Locate and identify every blood parasite.
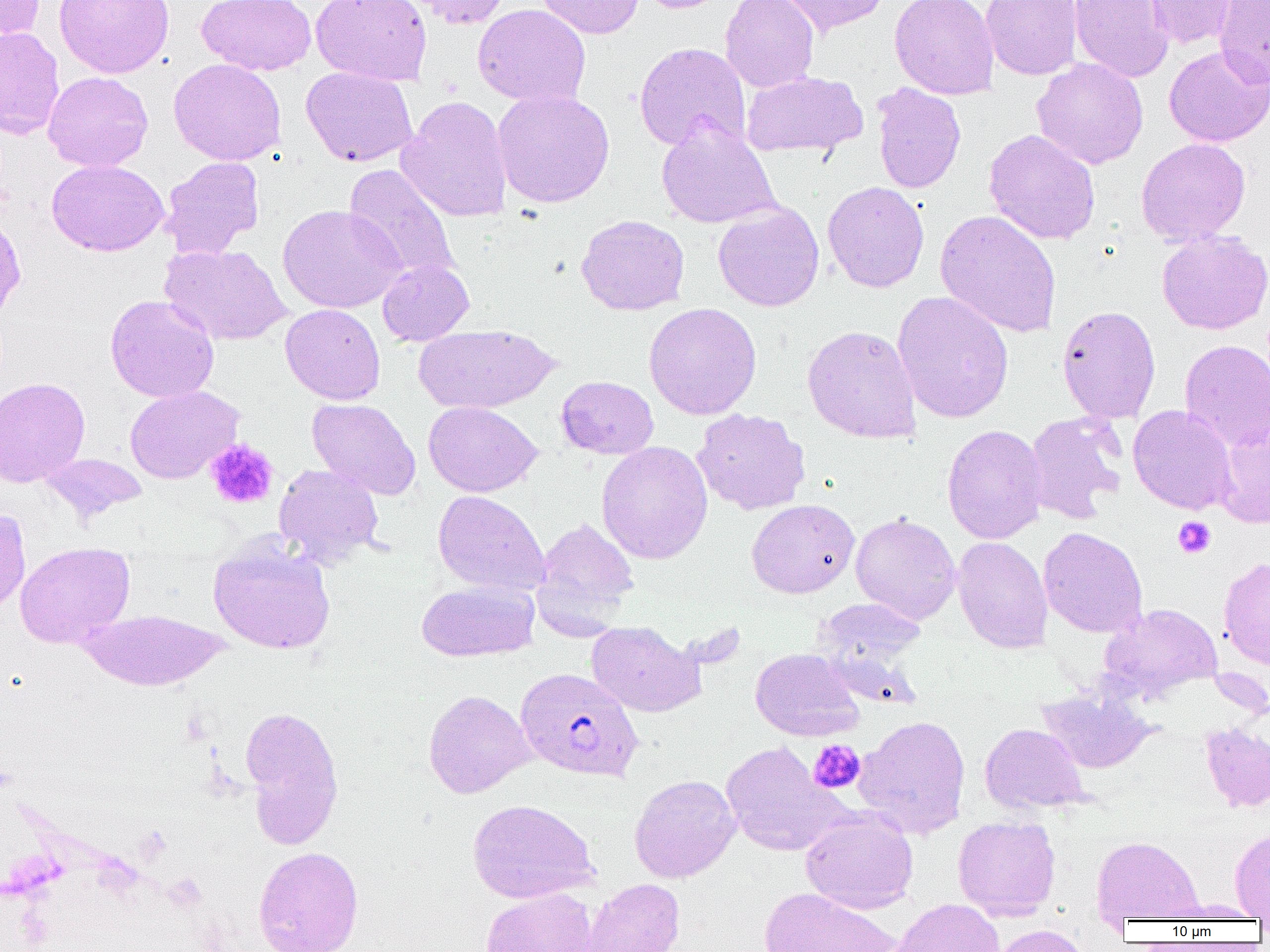
Approximate bounding boxes as (x1, y1, x2, y2) in pixels.
Plasmodium falciparum-infected red blood cells: (515, 667, 644, 782).
No Plasmodium ovale, Plasmodium malariae, Plasmodium vivax, Babesia divergens, or Trypanosoma brucei observed.

Uninfected red blood cell locations: (1, 0, 45, 42), (54, 0, 175, 79), (196, 0, 317, 76), (310, 0, 432, 86), (402, 0, 513, 29), (536, 0, 644, 38), (635, 0, 735, 14), (721, 0, 819, 92), (774, 0, 891, 37), (889, 0, 1000, 100), (981, 0, 1083, 80), (1070, 0, 1174, 83), (1145, 0, 1238, 49), (1214, 0, 1270, 88), (472, 4, 591, 108), (0, 27, 65, 139), (634, 42, 751, 151), (1163, 45, 1270, 147), (1031, 57, 1149, 170), (168, 58, 286, 165), (300, 66, 418, 167), (42, 71, 153, 172), (742, 71, 867, 157), (872, 82, 966, 193), (493, 88, 615, 208), (397, 95, 513, 222), (656, 120, 780, 228), (984, 129, 1100, 245), (1135, 137, 1251, 247), (160, 156, 265, 259), (47, 160, 169, 257), (343, 164, 461, 285), (822, 181, 929, 293), (713, 201, 824, 312), (277, 204, 406, 313), (934, 209, 1062, 338), (576, 214, 690, 316), (1156, 229, 1270, 335), (160, 243, 291, 346), (377, 259, 474, 345), (892, 290, 1014, 423), (105, 294, 219, 403), (643, 302, 762, 420), (280, 303, 385, 405), (1056, 305, 1161, 424), (414, 324, 561, 414), (802, 324, 922, 443), (1179, 339, 1270, 450), (556, 375, 659, 459), (0, 376, 90, 488), (124, 385, 243, 484), (307, 398, 421, 500), (423, 401, 543, 497), (1128, 404, 1238, 515), (692, 408, 811, 515), (1024, 411, 1127, 523), (1215, 421, 1270, 528), (942, 424, 1047, 544), (596, 441, 713, 564), (40, 453, 147, 522), (273, 463, 384, 566), (432, 489, 550, 595), (746, 499, 859, 599), (0, 507, 31, 615), (850, 513, 961, 625), (533, 516, 639, 633), (1038, 527, 1148, 638), (208, 536, 336, 655), (952, 536, 1053, 654), (14, 542, 135, 648), (1218, 556, 1270, 671), (416, 581, 539, 661), (813, 598, 926, 673), (1100, 603, 1223, 701), (80, 608, 229, 691), (586, 621, 706, 718), (750, 648, 864, 741), (1036, 688, 1156, 774), (423, 689, 534, 798), (239, 704, 345, 849), (854, 715, 971, 839), (1200, 722, 1270, 812), (979, 723, 1088, 815), (720, 741, 845, 857), (629, 774, 741, 882), (468, 798, 599, 903), (800, 808, 919, 914), (953, 815, 1061, 920), (1230, 828, 1270, 919), (1092, 835, 1203, 921), (253, 846, 364, 952), (580, 877, 685, 952), (759, 886, 902, 952), (480, 887, 597, 952), (891, 898, 1006, 952), (990, 925, 1091, 952). Platelet locations: (205, 439, 279, 509), (1173, 516, 1216, 559), (808, 740, 865, 794). Slide-level diagnosis: Plasmodium falciparum. Captured at 1000x magnification. Light microscopy. Image is 1270×952 pixels. Thin blood smear. One field of a larger specimen.